Identify the parasite.
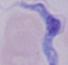

A trypanosome.

{
  "magnification": "1000x",
  "modality": "micrograph"
}